Report the malaria status of this cell.
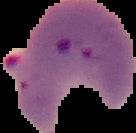
It is parasitized.

Summary:
  - Image size: 136×133 pixels
  - Preparation: thin blood film
  - Image type: segmented cell region on a black background